Report the malaria status of this cell.
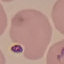
It is uninfected.

Acquired by smartphone through the microscope eyepiece. Giemsa stain. Thin smear of blood. Cell patch, automatically extracted from a larger field of view and resized to 64 × 64 pixels.